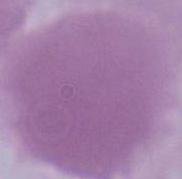

Captured at 1000x magnification. Micrograph. An erythrocyte is shown.